Locate every Plasmodium parasite.
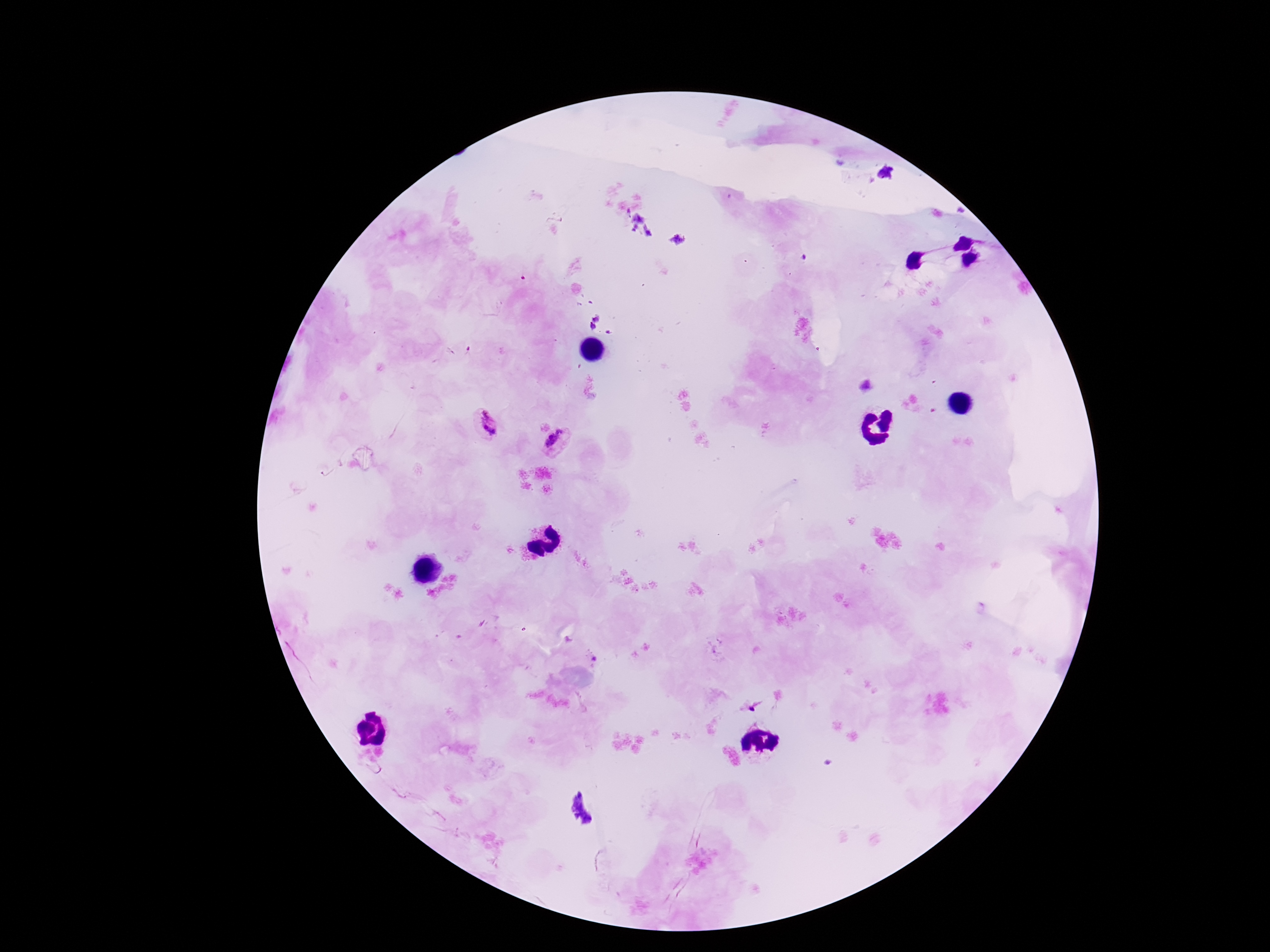
Approximate centers as {x, y} in pixels.
Plasmodium parasites: {488, 424}, {557, 443}.

capture = smartphone camera through the microscope eyepiece
field of view = one from this slide
patient malaria status = positive
stain = Giemsa
image size = 1270×952 pixels
preparation = thick peripheral-blood smear
magnification = 100x